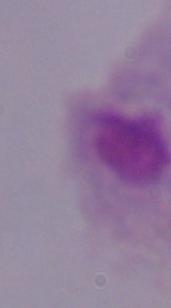

A trichomonad is shown. Micrograph. 1000x magnification.